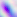 400x magnification. Micrograph. Toxoplasma gondii is seen.